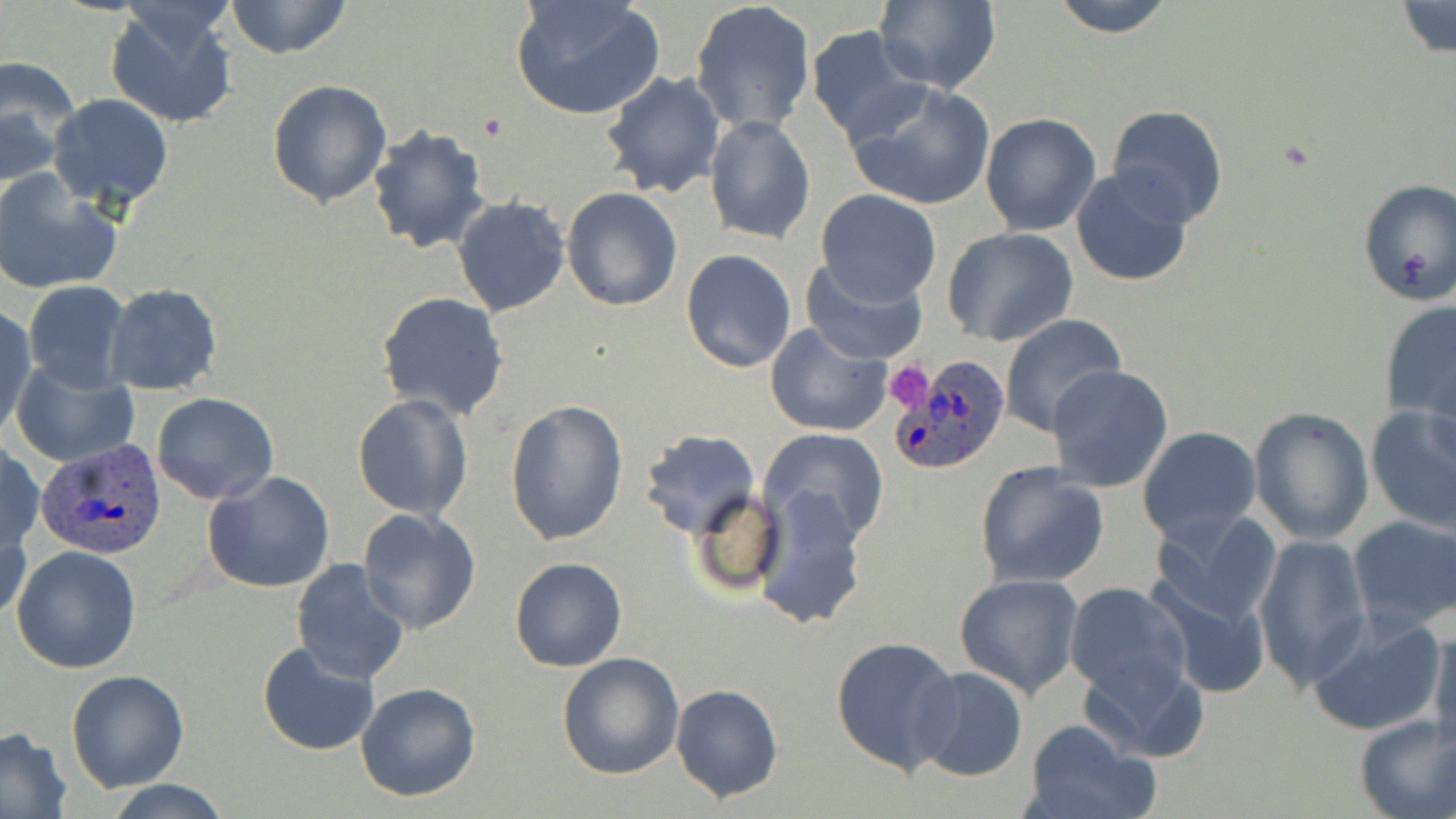
Summary:
  - Coordinate format: approximate bounding boxes as [x1, y1, x2, y2] in pixels
  - Uninfected red blood cell locations: [224, 0, 351, 60], [511, 0, 665, 120], [1048, 0, 1177, 38], [874, 1, 1001, 93], [1392, 1, 1456, 61], [691, 2, 818, 134], [103, 4, 239, 129], [805, 25, 923, 143], [0, 59, 79, 183], [601, 69, 726, 198], [267, 79, 393, 209], [843, 79, 996, 212], [47, 93, 174, 211], [1107, 105, 1228, 229], [979, 112, 1102, 237], [704, 113, 816, 245], [367, 124, 491, 253], [1070, 167, 1194, 287], [0, 168, 123, 296], [1356, 176, 1456, 308], [563, 187, 683, 312], [814, 190, 942, 306], [452, 196, 572, 317], [942, 227, 1080, 347], [681, 249, 797, 373], [800, 258, 929, 366], [23, 281, 132, 393], [102, 283, 222, 395], [375, 291, 510, 419], [1380, 299, 1456, 422], [1, 305, 36, 438], [997, 313, 1126, 437], [764, 320, 892, 438], [11, 361, 140, 468], [1049, 365, 1174, 493], [152, 393, 278, 505], [353, 393, 472, 521], [506, 400, 631, 546], [1364, 405, 1456, 534], [1248, 406, 1375, 545], [1136, 426, 1263, 549], [637, 428, 762, 537], [758, 428, 890, 546], [1, 444, 45, 554], [973, 460, 1109, 589], [203, 470, 336, 594], [752, 484, 868, 631], [688, 487, 786, 597], [1149, 506, 1283, 630], [357, 507, 482, 635], [1, 514, 32, 631], [1348, 515, 1456, 634], [1253, 533, 1372, 690], [11, 545, 142, 674], [509, 557, 628, 673], [290, 560, 410, 685], [1149, 565, 1277, 700], [954, 572, 1086, 699], [1064, 581, 1194, 703], [1308, 614, 1447, 738], [1428, 621, 1456, 756], [830, 634, 962, 775], [256, 643, 380, 756], [557, 651, 685, 779], [1078, 651, 1210, 762], [912, 667, 1028, 782], [66, 670, 192, 792], [355, 681, 483, 802], [670, 684, 783, 802], [1352, 714, 1456, 819], [1021, 719, 1155, 819], [1, 727, 71, 819], [103, 780, 233, 818]
  - Platelet locations: [882, 361, 935, 413]
  - Plasmodium ovale-infected red blood cell locations: [887, 352, 1013, 476], [37, 438, 168, 560]
  - Slide-level diagnosis: Plasmodium ovale
  - Modality: optical microscopy
  - Stain: May-Grünwald-Giemsa
  - Field of view: single
  - Magnification: 1000x
  - Preparation: thin blood film
  - Image size: 1456×819 pixels